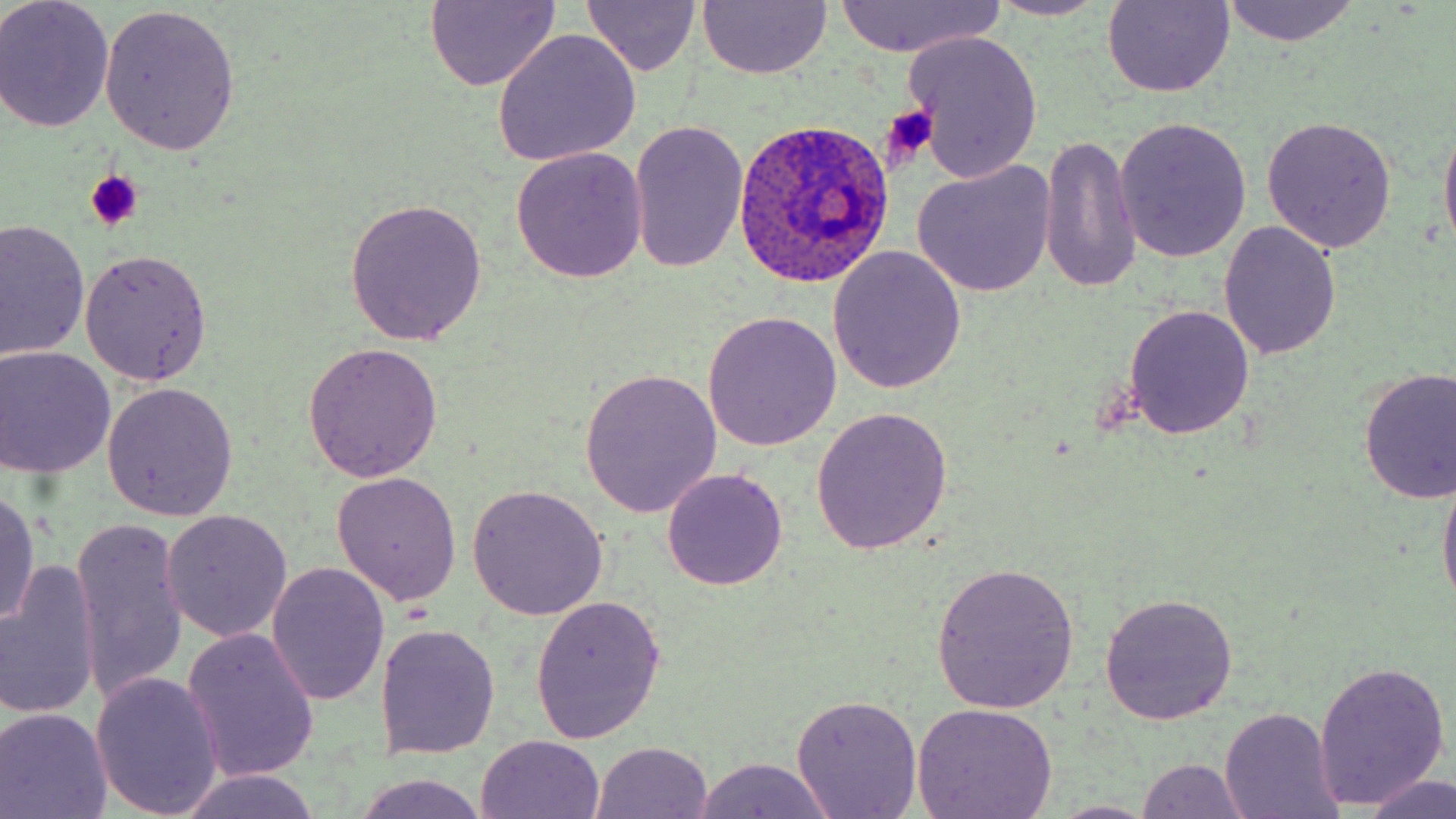
Plasmodium ovale-infected red blood cell locations = approximate bounding boxes as (x1, y1, x2, y2) in pixels: (733, 118, 894, 289)
slide-level diagnosis = Plasmodium ovale
field of view = one of a larger specimen
stain = May-Grünwald-Giemsa
preparation = thin blood film
uninfected red blood cell locations = approximate bounding boxes as (x1, y1, x2, y2) in pixels: (0, 0, 115, 132), (982, 0, 1114, 22), (424, 1, 562, 90), (1100, 1, 1236, 98), (1219, 1, 1360, 46), (697, 2, 832, 80), (829, 2, 1006, 57), (582, 3, 703, 77), (100, 5, 240, 156), (491, 29, 642, 166), (903, 31, 1046, 183), (1438, 108, 1456, 263), (1261, 116, 1396, 254), (1115, 117, 1251, 263), (627, 122, 748, 274), (1038, 136, 1144, 294), (511, 146, 648, 284), (912, 161, 1057, 298), (347, 198, 489, 345), (1, 219, 89, 366), (1219, 222, 1342, 360), (827, 246, 967, 395), (79, 249, 213, 385), (1123, 304, 1255, 440), (703, 309, 843, 452), (301, 343, 442, 482), (0, 346, 116, 478), (1356, 367, 1456, 505), (580, 368, 722, 517), (102, 382, 239, 521), (810, 405, 954, 553), (1437, 463, 1456, 616), (663, 469, 786, 589), (331, 471, 463, 606), (467, 485, 609, 619), (0, 488, 42, 631), (160, 512, 293, 644), (71, 520, 191, 705), (1, 560, 101, 723), (929, 560, 1080, 712), (267, 564, 389, 705), (1098, 591, 1238, 723), (530, 596, 667, 745), (376, 624, 501, 758), (182, 627, 321, 784), (1314, 660, 1451, 810), (91, 672, 224, 817), (791, 694, 923, 819), (910, 703, 1060, 819), (0, 706, 113, 819), (1217, 707, 1343, 819), (476, 734, 605, 818), (591, 742, 714, 819), (688, 756, 840, 818), (1134, 758, 1253, 818), (176, 769, 323, 819), (349, 772, 494, 819), (1362, 773, 1456, 819), (1048, 800, 1160, 818)
image size = 1456×819 pixels
modality = light microscopy
platelet locations = approximate bounding boxes as (x1, y1, x2, y2) in pixels: (879, 106, 938, 166), (85, 170, 144, 232)
magnification = 1000x